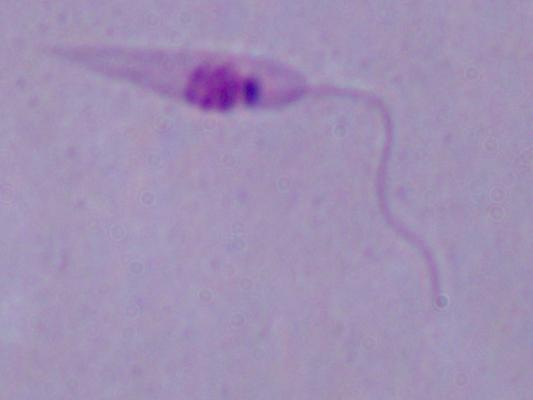 1000x magnification. A Leishmania parasite is shown. Micrograph.